Identify the blood parasite species.
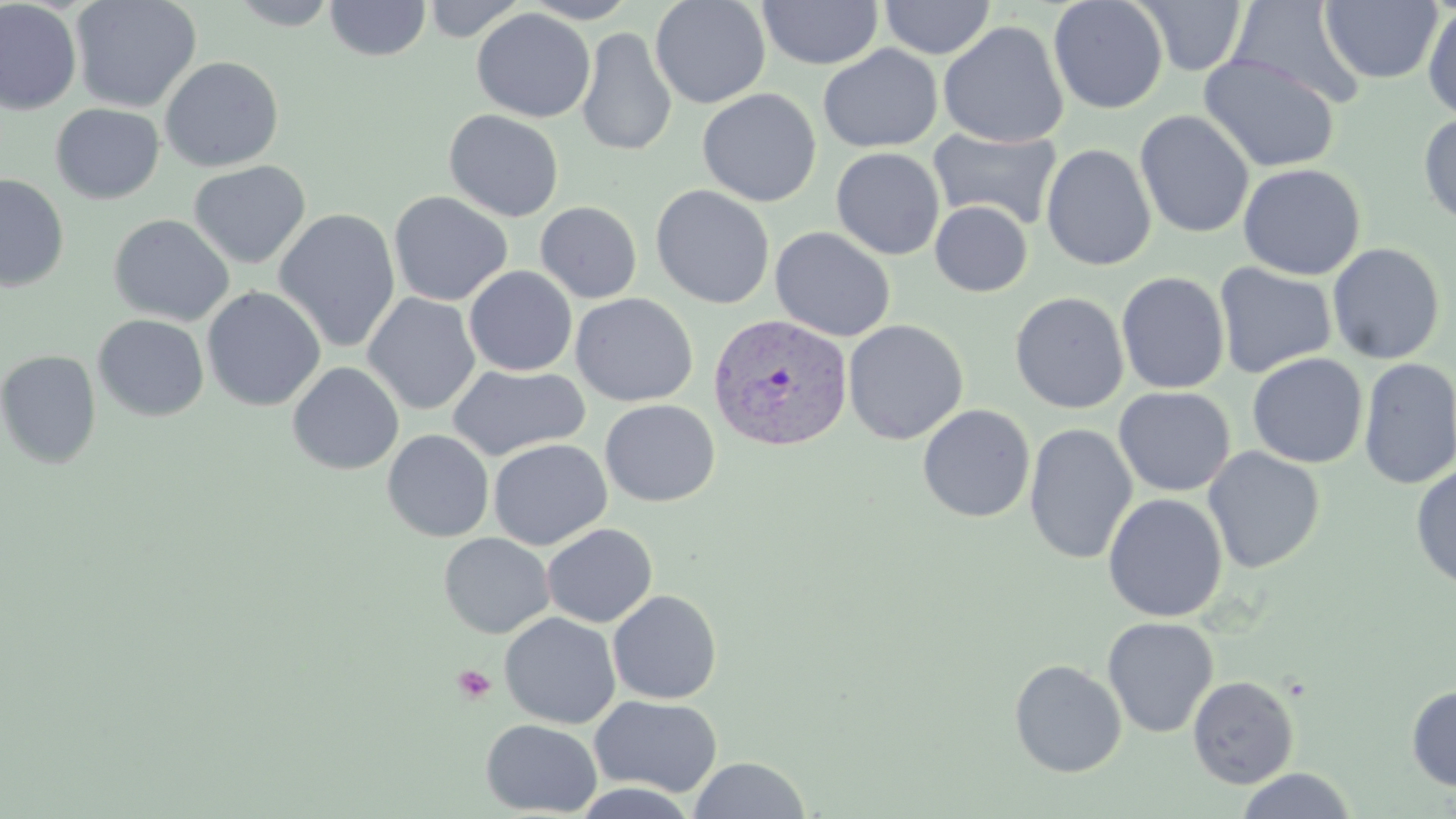

Plasmodium vivax.

Summary:
  - Coordinate format: approximate bounding boxes as (x1, y1, x2, y2) in pixels
  - Platelet locations: (453, 664, 497, 704)
  - Plasmodium vivax-infected red blood cell locations: (708, 313, 853, 452)
  - Uninfected red blood cell locations: (69, 0, 202, 113), (227, 0, 342, 30), (324, 0, 431, 62), (420, 0, 528, 41), (520, 0, 640, 23), (650, 0, 771, 109), (879, 0, 996, 59), (1048, 0, 1169, 115), (1136, 0, 1247, 76), (0, 1, 82, 115), (758, 1, 883, 70), (1226, 1, 1365, 108), (1319, 1, 1443, 85), (1423, 4, 1456, 123), (472, 8, 595, 123), (938, 21, 1069, 148), (576, 27, 677, 157), (818, 44, 943, 153), (1199, 54, 1340, 173), (159, 56, 284, 172), (697, 88, 822, 207), (50, 103, 164, 204), (444, 109, 565, 222), (1135, 110, 1254, 239), (1418, 112, 1456, 228), (927, 127, 1063, 230), (1041, 143, 1157, 271), (831, 147, 945, 260), (188, 160, 311, 269), (1238, 163, 1366, 280), (0, 173, 69, 291), (651, 184, 775, 309), (388, 190, 513, 306), (535, 201, 642, 303), (929, 201, 1033, 296), (273, 208, 401, 353), (108, 214, 235, 326), (769, 226, 896, 342), (1326, 242, 1446, 365), (1213, 262, 1337, 379), (464, 266, 577, 376), (1116, 271, 1230, 395), (202, 286, 326, 411), (1009, 291, 1129, 414), (363, 293, 480, 414), (570, 293, 698, 407), (93, 314, 209, 421), (843, 319, 968, 445), (0, 350, 101, 469), (1247, 353, 1368, 468), (1358, 358, 1456, 489), (286, 361, 404, 475), (447, 364, 591, 460), (1113, 386, 1236, 497), (600, 399, 720, 507), (917, 404, 1035, 523), (1024, 422, 1138, 565), (382, 430, 494, 542), (488, 438, 612, 550), (1203, 446, 1325, 573), (1410, 465, 1456, 592), (1103, 493, 1228, 622), (541, 523, 657, 627), (438, 532, 553, 638), (608, 589, 722, 704), (499, 612, 621, 728), (1102, 616, 1219, 738), (1009, 659, 1127, 778), (1187, 675, 1300, 789), (1406, 684, 1456, 791), (589, 695, 723, 797), (481, 719, 602, 817), (689, 755, 811, 818), (1235, 768, 1358, 819), (570, 783, 700, 818)
  - Modality: optical microscopy
  - Magnification: 1000x
  - Stain: May-Grünwald-Giemsa
  - Preparation: thin blood film
  - Image size: 1456×819 pixels
  - Field of view: single